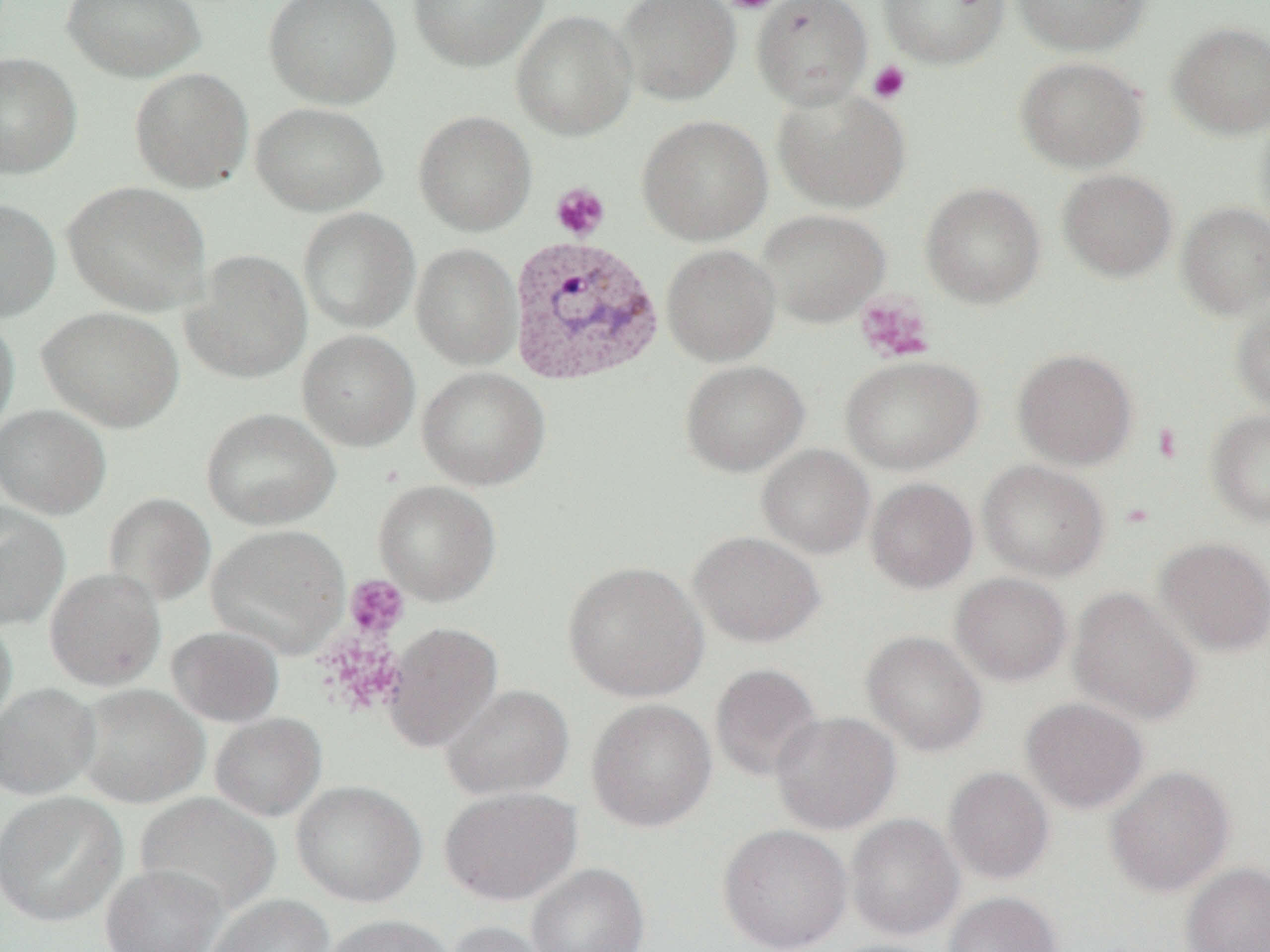
Approximate bounding boxes as (x1, y1, x2, y2) in pixels. Uninfected red blood cell locations: (62, 0, 206, 82), (264, 0, 402, 109), (408, 0, 548, 70), (616, 0, 741, 105), (752, 0, 873, 109), (878, 0, 1009, 68), (1012, 0, 1150, 57), (511, 9, 637, 141), (1167, 21, 1270, 139), (0, 51, 82, 179), (1015, 56, 1148, 173), (130, 67, 253, 193), (772, 88, 911, 214), (250, 102, 388, 215), (414, 110, 536, 236), (1254, 111, 1270, 240), (637, 115, 773, 245), (1057, 168, 1177, 282), (63, 181, 210, 315), (921, 182, 1045, 308), (0, 198, 61, 322), (1176, 201, 1270, 320), (298, 208, 420, 333), (756, 209, 890, 327), (411, 243, 521, 369), (661, 244, 780, 366), (182, 249, 313, 383), (38, 305, 184, 432), (1231, 305, 1270, 414), (0, 313, 19, 443), (298, 329, 420, 451), (1013, 348, 1138, 470), (840, 355, 983, 474), (680, 360, 809, 476), (417, 367, 550, 491), (0, 404, 111, 519), (201, 408, 341, 530), (1207, 409, 1270, 526), (757, 444, 875, 558), (978, 459, 1109, 581), (866, 478, 978, 593), (374, 480, 502, 605), (104, 492, 216, 607), (0, 502, 70, 630), (207, 523, 350, 658), (689, 531, 824, 647), (1155, 537, 1270, 657), (562, 560, 709, 702), (44, 567, 166, 690), (950, 572, 1072, 685), (1068, 587, 1201, 725), (0, 611, 17, 736), (383, 621, 503, 753), (166, 625, 285, 726), (861, 630, 988, 756), (710, 663, 824, 782), (0, 683, 100, 800), (75, 684, 208, 808), (441, 684, 574, 800), (1021, 697, 1149, 814), (586, 698, 717, 833), (770, 711, 901, 834), (210, 712, 327, 821), (1106, 765, 1235, 897), (943, 766, 1055, 885), (292, 780, 427, 906), (439, 786, 583, 906), (0, 791, 128, 926), (136, 792, 280, 916), (845, 813, 964, 940), (717, 824, 852, 952), (526, 862, 649, 952), (1181, 862, 1270, 952), (100, 863, 228, 952), (942, 891, 1062, 952), (207, 894, 333, 952), (320, 914, 456, 952), (445, 920, 555, 952). Platelet locations: (723, 0, 778, 14), (867, 61, 911, 104), (550, 182, 610, 241), (855, 293, 936, 363), (1152, 422, 1183, 464), (345, 575, 409, 639). Plasmodium vivax-infected red blood cell locations: (507, 234, 665, 388). Slide-level diagnosis: Plasmodium vivax. Single field of view. Optical microscopy. Thin blood smear. Image is 1270×952 pixels. 1000x magnification.